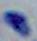
Summary:
  - Identification: Toxoplasma gondii
  - Modality: photomicrograph
  - Magnification: 1000x